Identify the parasite.
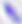
Toxoplasma gondii.

magnification = 400x
modality = photomicrograph